Give the extent of all uninfected red blood cells.
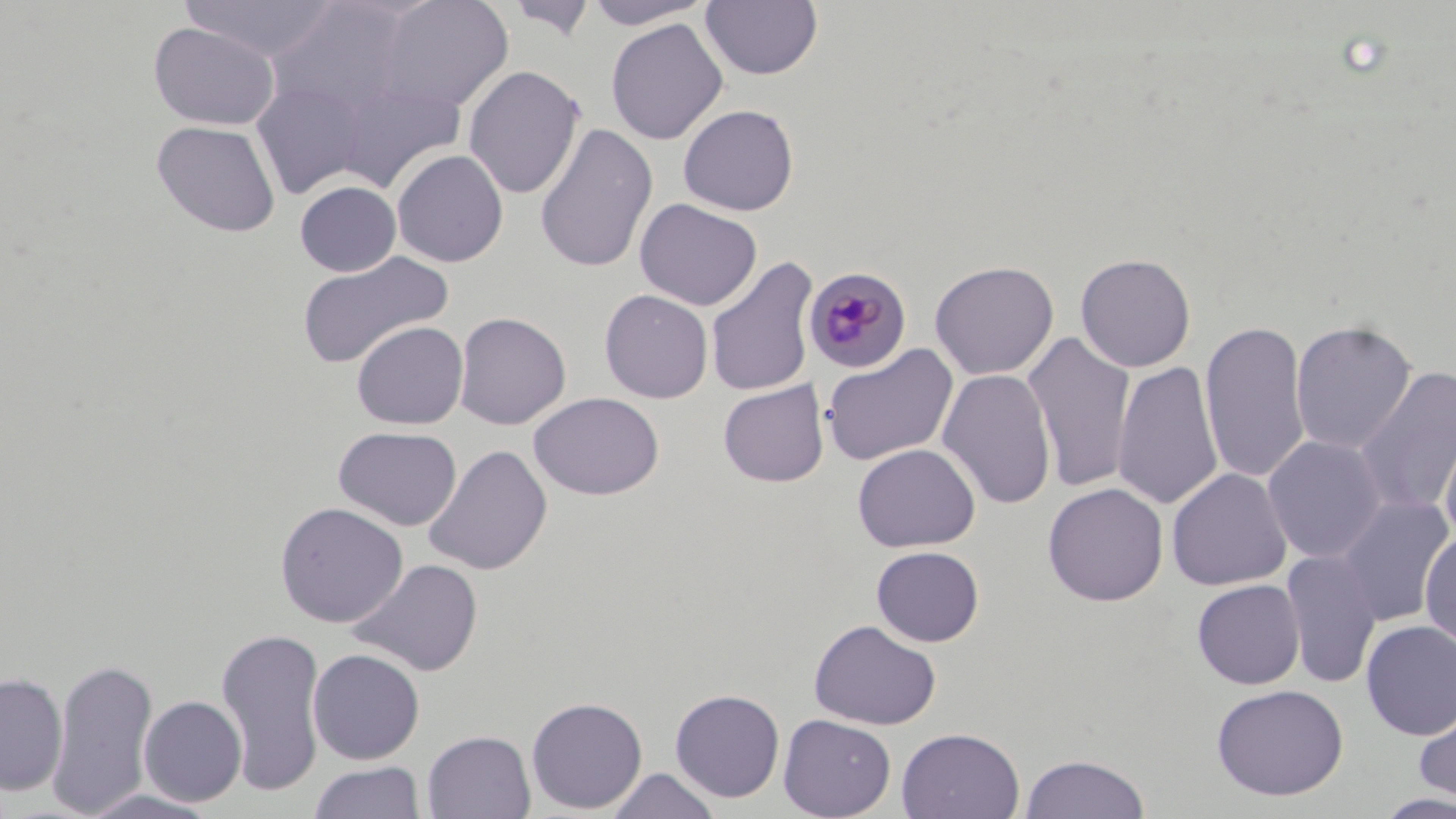
Approximate bounding boxes as (x1, y1, x2, y2) in pixels.
Uninfected red blood cells: (181, 0, 341, 62), (373, 0, 514, 113), (506, 0, 597, 41), (582, 0, 715, 29), (263, 1, 418, 120), (700, 1, 823, 81), (605, 18, 729, 145), (148, 21, 280, 130), (463, 65, 585, 200), (252, 81, 369, 200), (334, 81, 466, 193), (678, 104, 799, 216), (151, 119, 281, 238), (533, 121, 658, 273), (391, 149, 509, 267), (295, 181, 401, 277), (634, 198, 762, 311), (295, 250, 453, 370), (1075, 253, 1196, 373), (705, 256, 819, 398), (929, 260, 1059, 380), (599, 289, 713, 404), (453, 311, 571, 429), (1200, 319, 1311, 485), (1290, 319, 1417, 454), (351, 321, 468, 429), (1022, 331, 1137, 494), (820, 343, 959, 466), (1113, 360, 1224, 511), (1354, 365, 1456, 518), (937, 368, 1057, 510), (718, 380, 829, 487), (529, 391, 665, 500), (1437, 410, 1456, 547), (333, 426, 462, 531), (1262, 434, 1388, 563), (852, 443, 980, 552), (423, 444, 553, 576), (1166, 467, 1292, 590), (1042, 482, 1169, 606), (1334, 495, 1454, 626), (275, 501, 408, 628), (1420, 528, 1456, 651), (871, 546, 984, 647), (1281, 550, 1383, 689), (348, 558, 483, 678), (1192, 579, 1305, 689), (809, 620, 941, 730), (1360, 620, 1456, 741), (215, 626, 328, 798), (307, 648, 425, 765), (46, 657, 159, 816), (0, 671, 67, 796), (1211, 683, 1349, 801), (669, 688, 785, 803), (139, 695, 247, 806), (526, 696, 648, 814), (1414, 700, 1456, 806), (778, 714, 896, 819), (896, 727, 1025, 819), (422, 730, 536, 819), (1019, 753, 1149, 818), (309, 761, 427, 819), (606, 768, 721, 819), (78, 789, 224, 818), (1375, 792, 1456, 818).

Summary:
  - Plasmodium malariae-infected red blood cell locations: (804, 267, 912, 374)
  - Slide-level diagnosis: Plasmodium malariae
  - Preparation: thin blood film
  - Field of view: single
  - Image size: 1456×819 pixels
  - Modality: light microscopy
  - Magnification: 1000x
  - Stain: May-Grünwald-Giemsa